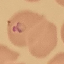
result: malaria parasites detected
capture: smartphone through the microscope eyepiece
stain: Giemsa
preparation: thin blood film
image_type: cell patch, automatically extracted from a larger field of view and resized to 64 × 64 pixels